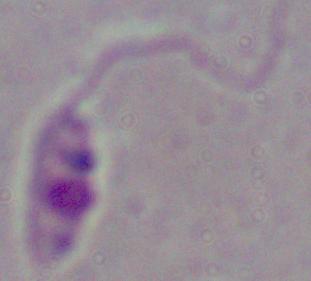

A Leishmania parasite is seen. Photomicrograph. 1000x magnification.